Identify the parasite.
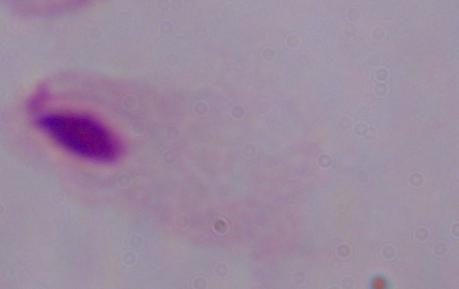
This is a trichomonad.

Captured at 1000x magnification. Micrograph.